Locate every Plasmodium malariae-infected red blood cell.
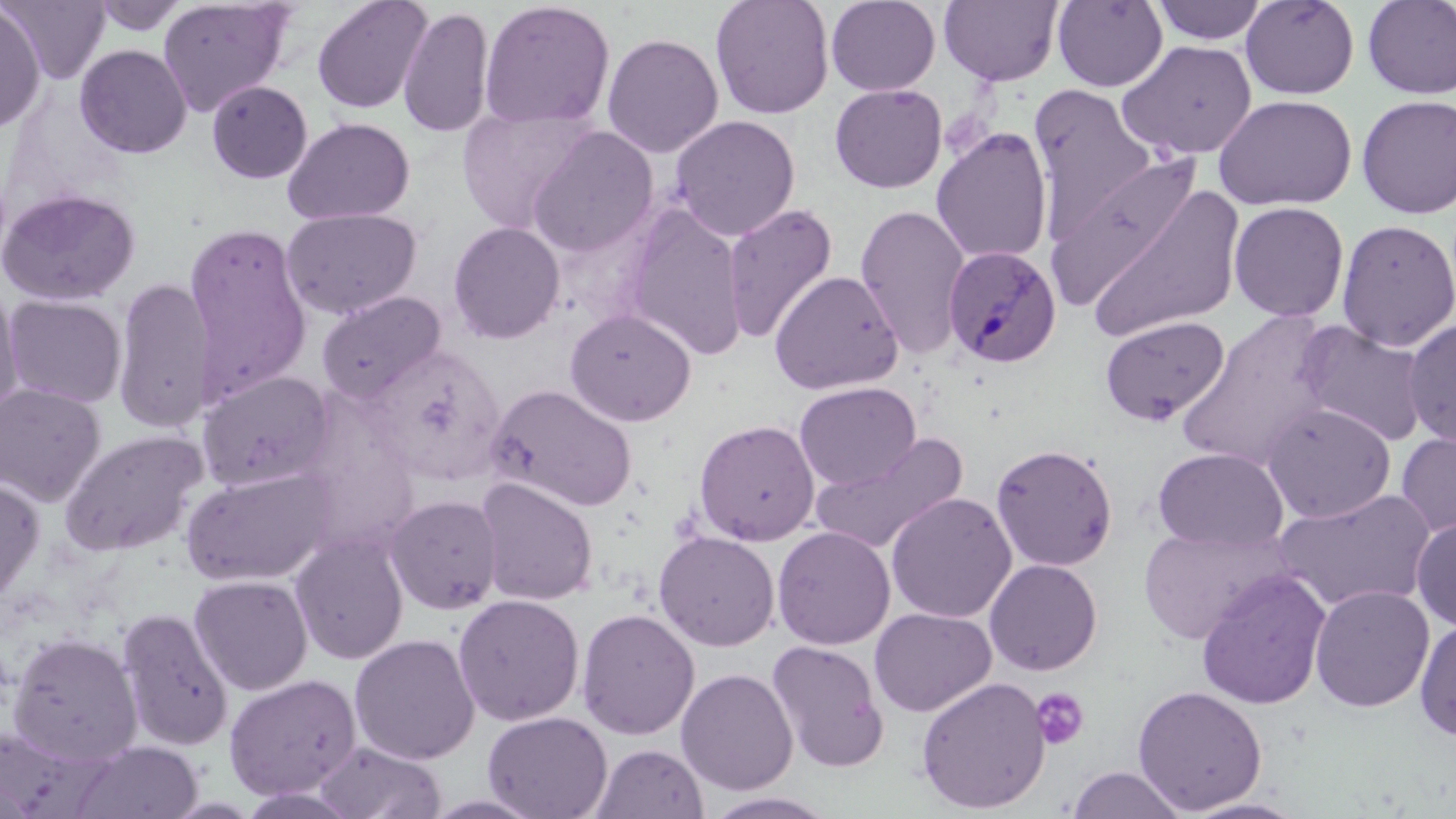

Approximate bounding boxes as [x1, y1, x2, y2] in pixels.
Plasmodium malariae-infected red blood cells: [943, 245, 1061, 369].

slide-level diagnosis = Plasmodium malariae
platelet locations = approximate bounding boxes as [x1, y1, x2, y2] in pixels: [1030, 687, 1090, 750]
field of view = one of a larger specimen
image size = 1456×819 pixels
magnification = 1000x
preparation = thin blood smear
uninfected red blood cell locations = approximate bounding boxes as [x1, y1, x2, y2] in pixels: [2, 0, 110, 84], [156, 0, 294, 116], [310, 0, 433, 114], [710, 0, 835, 120], [826, 0, 941, 96], [939, 0, 1063, 87], [1052, 0, 1168, 92], [1240, 0, 1360, 99], [88, 1, 193, 37], [479, 1, 616, 129], [1149, 1, 1268, 45], [1361, 1, 1456, 99], [0, 3, 45, 133], [398, 6, 495, 139], [601, 32, 724, 158], [1119, 40, 1258, 161], [75, 44, 192, 158], [206, 79, 313, 184], [829, 83, 947, 193], [1028, 83, 1157, 230], [1213, 94, 1357, 211], [1356, 95, 1456, 219], [457, 105, 598, 233], [669, 115, 801, 241], [282, 117, 416, 225], [526, 126, 659, 258], [931, 127, 1053, 265], [1075, 175, 1248, 344], [0, 187, 141, 306], [721, 202, 839, 346], [1228, 202, 1349, 322], [621, 204, 749, 361], [854, 205, 970, 360], [281, 207, 422, 320], [1336, 219, 1455, 352], [447, 221, 566, 344], [183, 222, 313, 400], [769, 270, 903, 395], [111, 277, 210, 433], [0, 281, 23, 424], [316, 290, 447, 403], [4, 294, 128, 409], [564, 307, 696, 427], [1177, 311, 1337, 471], [1099, 315, 1229, 426], [1403, 318, 1456, 449], [1296, 322, 1430, 447], [370, 343, 508, 486], [198, 371, 335, 492], [794, 382, 920, 491], [0, 383, 106, 506], [486, 384, 637, 512], [1261, 402, 1397, 523], [694, 419, 820, 545], [58, 429, 208, 557], [1395, 430, 1456, 540], [810, 433, 969, 555], [990, 442, 1119, 572], [1152, 447, 1288, 552], [181, 466, 337, 587], [0, 475, 45, 609], [474, 477, 598, 606], [1272, 488, 1437, 613], [885, 491, 1016, 623], [385, 494, 503, 614], [1411, 516, 1456, 631], [1137, 524, 1294, 644], [772, 526, 895, 649], [653, 530, 780, 651], [290, 532, 409, 665], [984, 559, 1102, 676], [1195, 569, 1332, 710], [189, 574, 313, 696], [1309, 584, 1435, 712], [452, 594, 584, 726], [116, 606, 234, 752], [869, 607, 996, 716], [576, 608, 700, 740], [1414, 618, 1456, 743], [6, 631, 143, 765], [349, 633, 480, 765], [767, 640, 889, 772], [676, 668, 798, 796], [223, 673, 361, 800], [915, 676, 1051, 814], [1131, 684, 1268, 814], [482, 710, 612, 819], [313, 740, 447, 819], [70, 741, 203, 819], [591, 743, 709, 819], [1066, 766, 1188, 819], [702, 791, 841, 818], [1180, 797, 1310, 819]
stain = May-Grünwald-Giemsa
modality = light microscopy